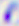 Toxoplasma gondii is seen. 400x magnification. Photomicrograph.